Give the preparation type.
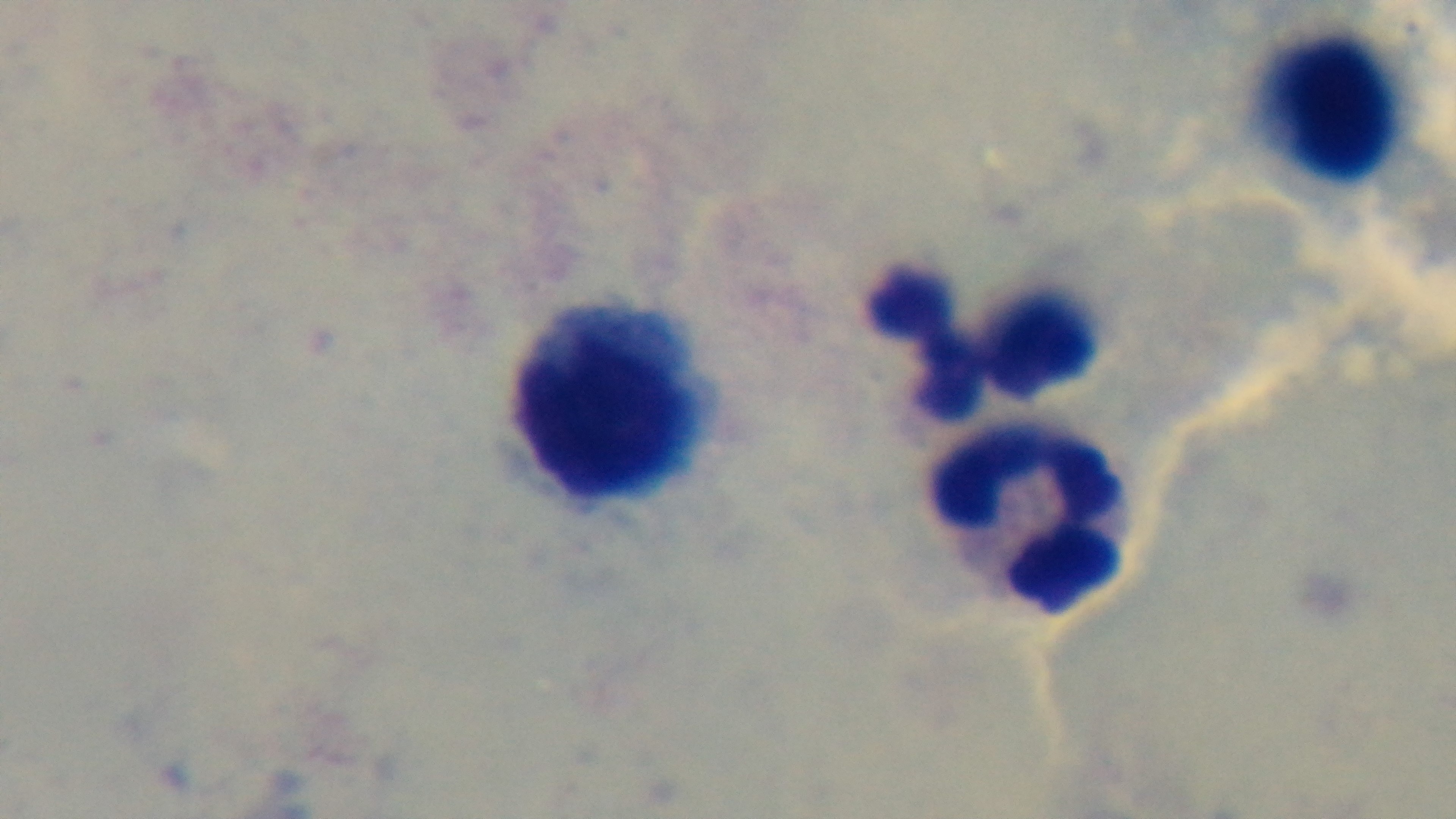
Thick.

Photomicrograph. Oil-immersion objective, 100x. Malaria status: uninfected. Single field of view. Mounted 4K digital camera. Giemsa stain.